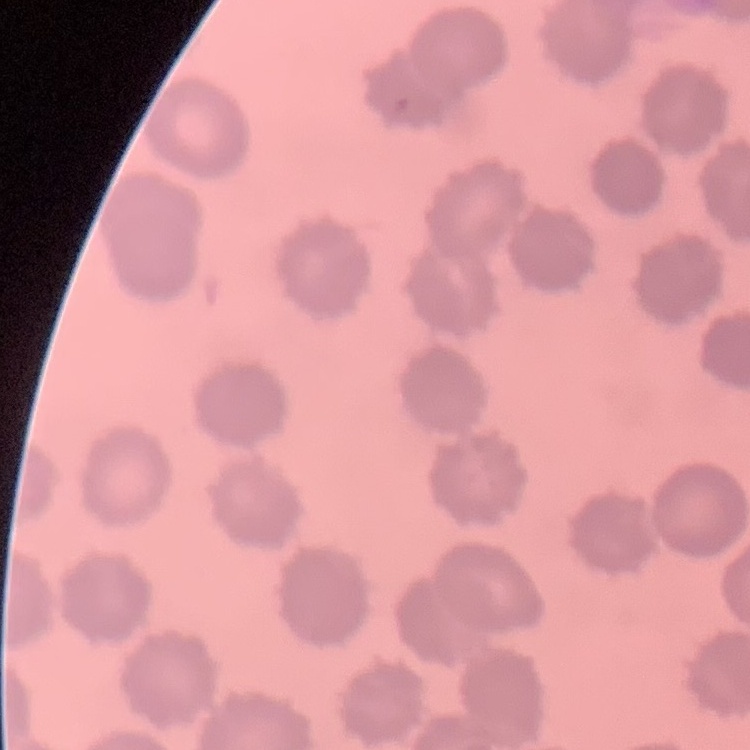
Summary:
  - Red blood cell morphology: no rouleaux formation
  - Stain: Field's or Giemsa
  - Preparation: thin peripheral smear
  - Image type: one tile cut from a larger photomicrograph